Name the cell type shown.
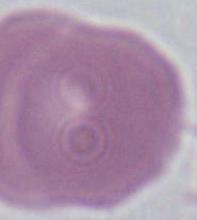
An erythrocyte.

modality = photomicrograph
magnification = 1000x